Locate every uninfected red blood cell.
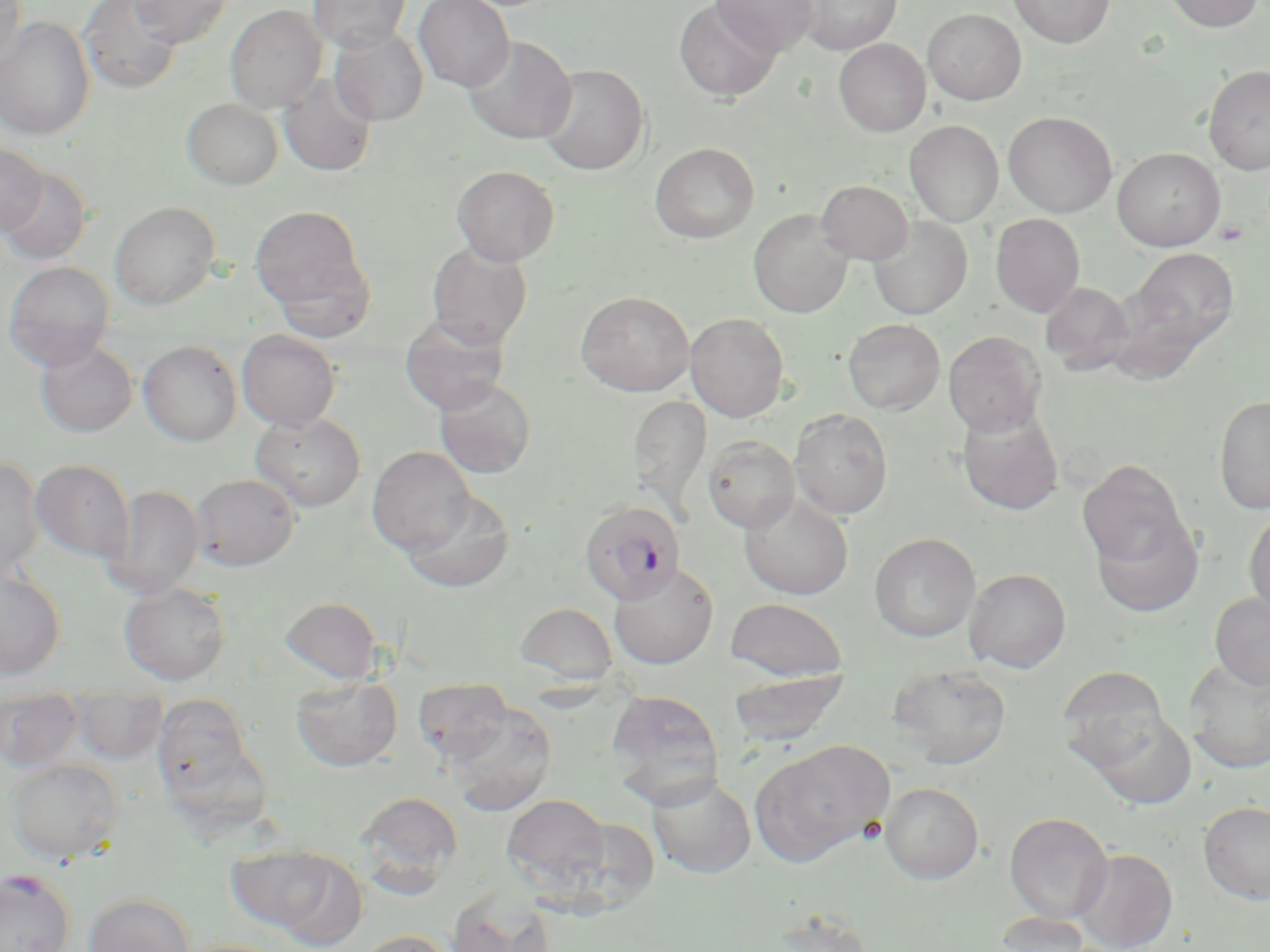

Approximate bounding boxes as [x1, y1, x2, y2] in pixels.
Uninfected red blood cells: [0, 0, 25, 66], [78, 0, 184, 95], [129, 0, 235, 48], [308, 0, 410, 52], [414, 0, 514, 92], [673, 0, 781, 102], [711, 0, 819, 56], [799, 0, 901, 54], [1008, 0, 1115, 49], [1164, 0, 1265, 33], [225, 5, 326, 112], [922, 7, 1026, 105], [0, 16, 95, 140], [329, 26, 429, 126], [463, 36, 576, 144], [833, 38, 931, 137], [538, 64, 649, 176], [1203, 64, 1270, 175], [279, 73, 377, 177], [182, 98, 283, 189], [1003, 111, 1117, 217], [905, 120, 1004, 226], [649, 142, 760, 243], [0, 144, 48, 235], [1112, 148, 1225, 251], [452, 165, 560, 266], [0, 167, 92, 265], [816, 179, 914, 265], [109, 201, 220, 309], [249, 203, 374, 326], [749, 209, 853, 318], [990, 213, 1085, 317], [868, 215, 972, 320], [427, 242, 532, 348], [1129, 246, 1239, 354], [3, 261, 115, 371], [1040, 281, 1135, 375], [575, 291, 695, 396], [685, 313, 790, 421], [399, 314, 510, 415], [843, 318, 945, 415], [237, 330, 341, 431], [943, 330, 1047, 436], [35, 338, 138, 437], [138, 340, 242, 446], [434, 377, 536, 479], [628, 395, 712, 516], [1213, 395, 1270, 515], [957, 408, 1064, 516], [790, 409, 893, 520], [250, 412, 366, 512], [703, 435, 800, 533], [367, 446, 475, 554], [0, 456, 45, 578], [31, 459, 134, 562], [1077, 459, 1189, 568], [191, 473, 299, 571], [103, 485, 205, 598], [401, 489, 515, 593], [739, 491, 854, 600], [1244, 511, 1270, 617], [1090, 512, 1204, 619], [869, 533, 981, 642], [609, 562, 719, 669], [0, 568, 66, 678], [964, 568, 1071, 673], [119, 581, 231, 686], [1209, 591, 1270, 691], [278, 596, 383, 683], [725, 597, 849, 683], [515, 601, 619, 685], [1184, 661, 1270, 773], [888, 663, 1012, 769], [1057, 666, 1170, 766], [727, 669, 849, 747], [291, 674, 402, 771], [412, 678, 514, 763], [605, 690, 725, 806], [0, 691, 83, 771], [152, 693, 255, 797], [71, 694, 167, 763], [445, 703, 557, 817], [1086, 710, 1197, 810], [751, 739, 892, 866], [4, 758, 123, 865], [647, 775, 756, 878], [880, 782, 984, 884], [354, 790, 464, 896], [502, 794, 610, 888], [1198, 801, 1270, 904], [1004, 812, 1113, 923], [230, 844, 362, 942], [1072, 847, 1178, 951], [0, 870, 76, 952], [447, 888, 555, 952], [83, 892, 195, 952], [765, 906, 876, 952], [990, 913, 1104, 952], [356, 930, 458, 952], [172, 939, 293, 952].

plasmodium_falciparum_infected_red_blood_cell_locations: 'approximate bounding boxes as [x1, y1, x2, y2] in pixels: [579, 500, 685, 604]'
slide_level_diagnosis: Plasmodium falciparum
field_of_view: one of a larger specimen
magnification: 1000x
image_size: 1270×952 pixels
preparation: thin blood smear
stain: May-Grünwald-Giemsa
modality: light microscopy